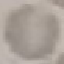
Summary:
  - Result: no malaria parasites detected
  - Image type: cell patch, automatically extracted from a larger field of view and resized to 64 × 64 pixels
  - Capture: smartphone camera at the microscope eyepiece
  - Stain: Giemsa
  - Preparation: thin blood film